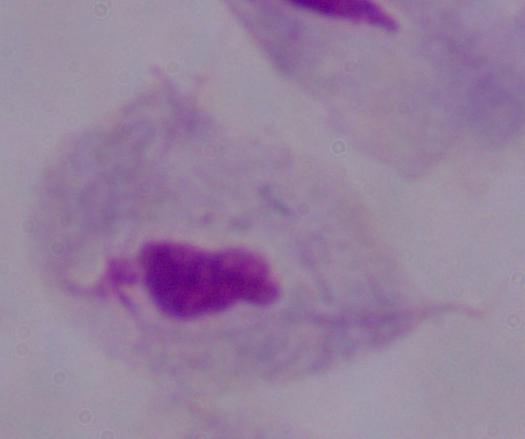 Captured at 1000x magnification. Photomicrograph. A trichomonad is seen.